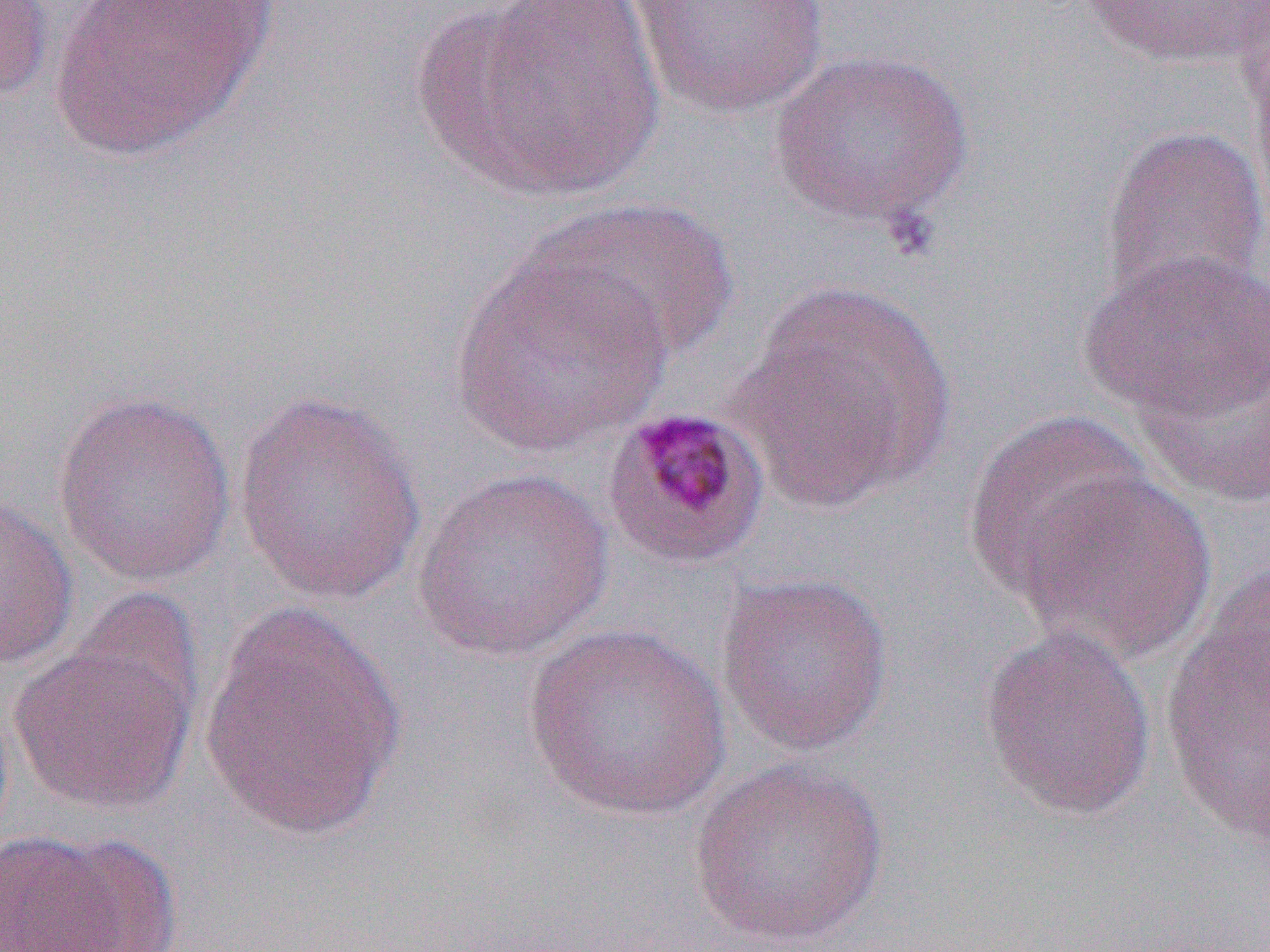

slide-level diagnosis = Plasmodium malariae
modality = optical microscopy
preparation = thin blood smear
Plasmodium malariae-infected red blood cell locations = approximate bounding boxes as (x1, y1, x2, y2) in pixels: (599, 403, 773, 571)
image size = 1270×952 pixels
field of view = single
magnification = 1000x
uninfected red blood cell locations = approximate bounding boxes as (x1, y1, x2, y2) in pixels: (0, 0, 54, 107), (432, 0, 666, 201), (1078, 0, 1269, 70), (48, 1, 271, 160), (626, 1, 831, 120), (769, 47, 974, 230), (1099, 123, 1269, 310), (537, 195, 738, 364), (450, 243, 674, 460), (1080, 247, 1270, 423), (735, 278, 958, 510), (1133, 343, 1269, 509), (233, 387, 429, 606), (51, 388, 238, 586), (963, 409, 1157, 602), (412, 468, 615, 663), (1012, 468, 1218, 664), (0, 495, 78, 672), (1157, 566, 1270, 845), (713, 570, 895, 756), (199, 598, 404, 841), (978, 623, 1158, 822), (522, 624, 733, 823), (9, 635, 196, 815), (688, 756, 891, 948), (1, 829, 131, 951)